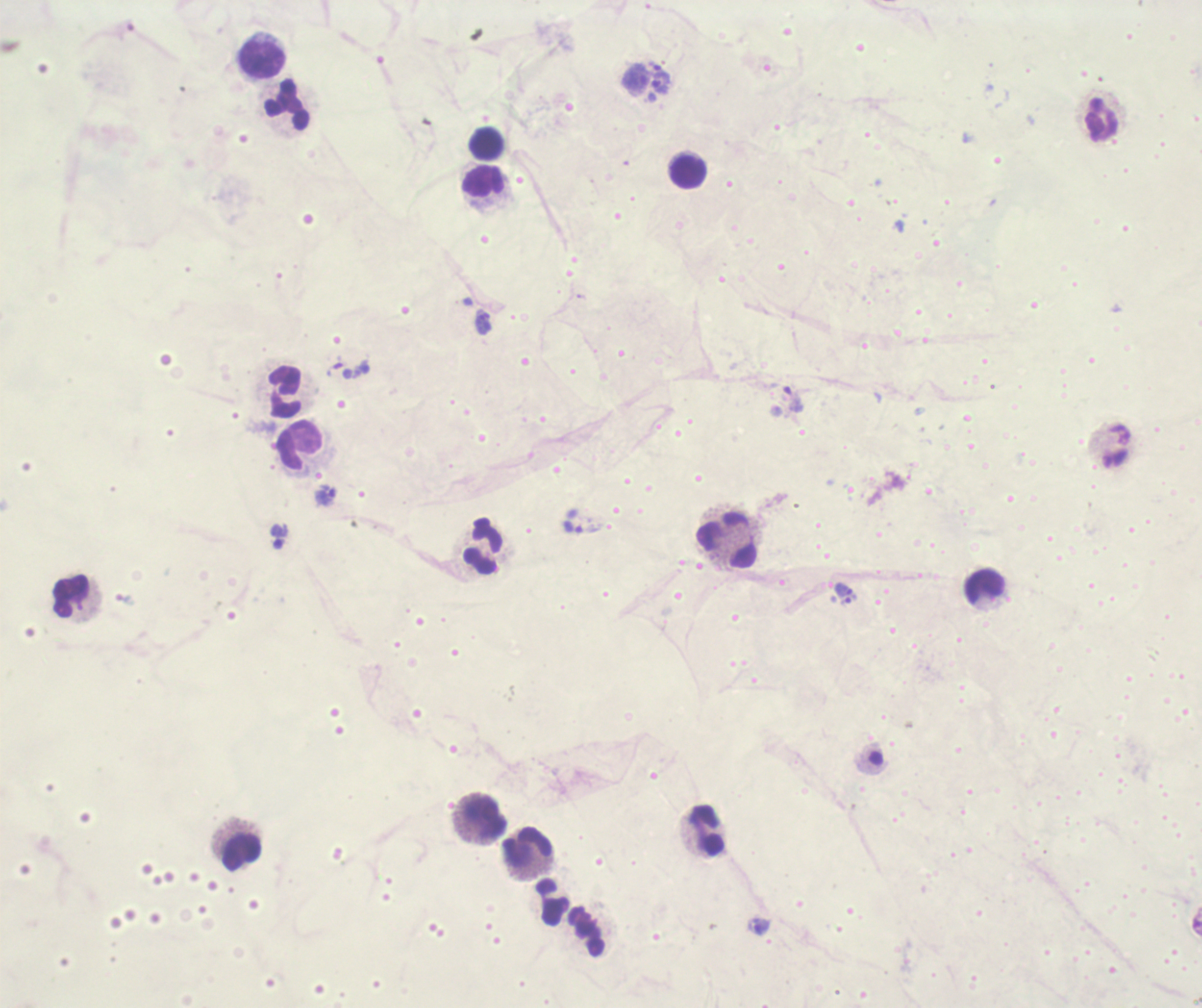
Approximate centers as (x, y) in pixels.
Summary:
  - Trophozoite locations: (635, 79), (662, 84), (574, 528), (845, 592)
  - Leukocyte locations: (260, 58), (286, 105), (1102, 120), (487, 142), (688, 172), (484, 182), (285, 392), (299, 445), (727, 541), (484, 547), (984, 586), (70, 597), (484, 817), (706, 831), (528, 848), (241, 853), (552, 902), (587, 932)
  - Context: previously used in an actual diagnosis
  - Background quality: unsatisfactory
  - Preparation: thick blood smear
  - Magnification: 100x
  - Coloration quality: bad
  - Stain: Romanowsky
  - Image size: 1202×1008 pixels
  - Result: malaria parasites detected
  - Field of view: one from this slide